Locate platelets.
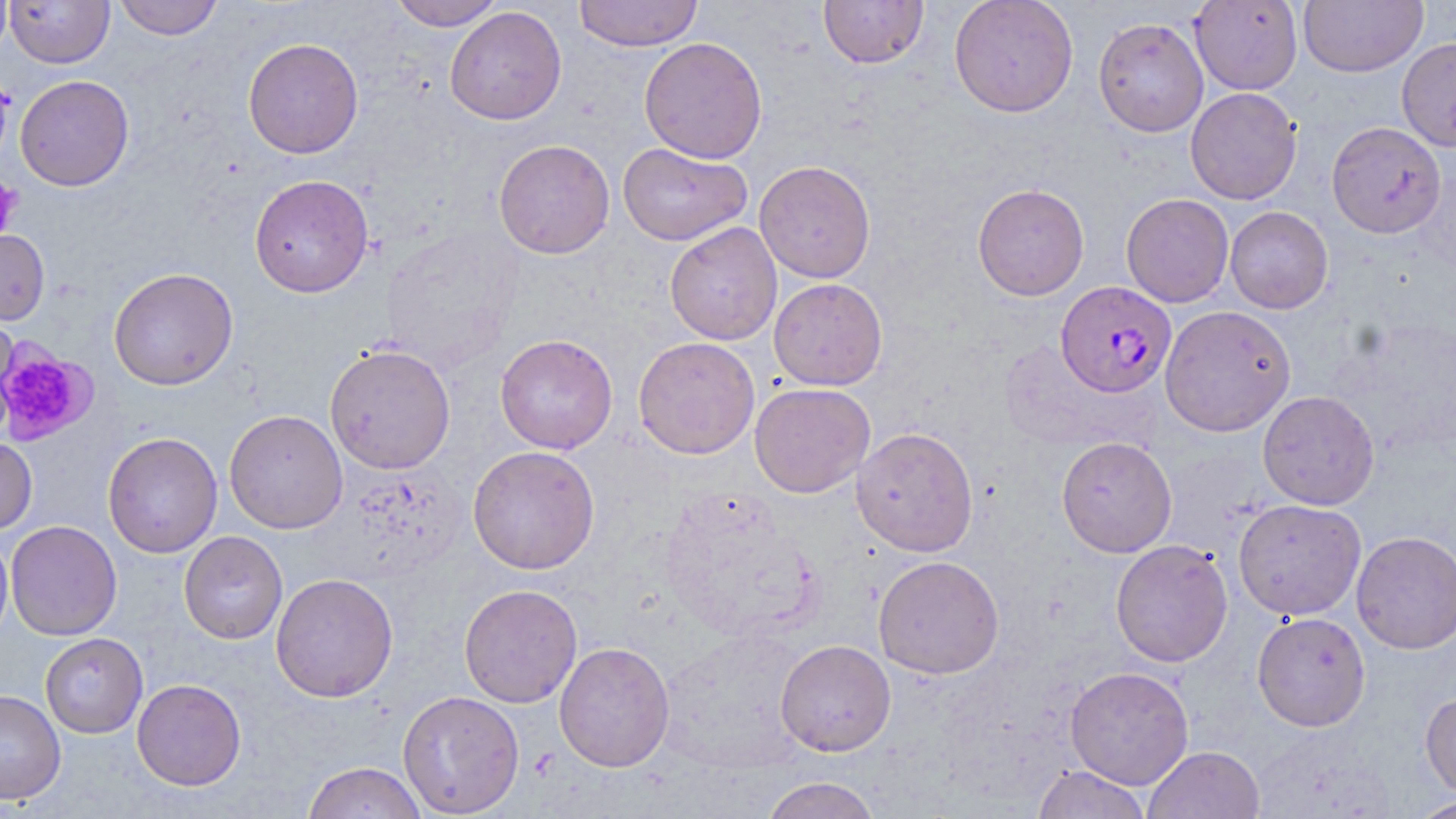

Approximate bounding boxes as named x1/y1/x2/y2 corners in pixels.
Platelets: (x1=0, y1=177, x2=22, y2=238), (x1=0, y1=340, x2=97, y2=447).

Summary:
  - Uninfected red blood cell locations: (x1=5, y1=0, x2=115, y2=68), (x1=114, y1=0, x2=223, y2=40), (x1=387, y1=0, x2=506, y2=30), (x1=573, y1=0, x2=704, y2=51), (x1=818, y1=0, x2=929, y2=69), (x1=949, y1=0, x2=1078, y2=117), (x1=1190, y1=1, x2=1302, y2=94), (x1=1298, y1=1, x2=1428, y2=76), (x1=444, y1=7, x2=566, y2=125), (x1=1093, y1=17, x2=1208, y2=137), (x1=639, y1=37, x2=767, y2=164), (x1=1397, y1=37, x2=1456, y2=151), (x1=243, y1=38, x2=363, y2=159), (x1=15, y1=74, x2=134, y2=191), (x1=1186, y1=87, x2=1302, y2=205), (x1=1326, y1=121, x2=1447, y2=238), (x1=493, y1=139, x2=615, y2=259), (x1=617, y1=143, x2=752, y2=246), (x1=754, y1=160, x2=876, y2=283), (x1=249, y1=174, x2=374, y2=298), (x1=972, y1=183, x2=1089, y2=300), (x1=1121, y1=193, x2=1234, y2=308), (x1=1225, y1=206, x2=1333, y2=313), (x1=664, y1=222, x2=782, y2=345), (x1=379, y1=226, x2=524, y2=372), (x1=0, y1=228, x2=49, y2=325), (x1=108, y1=267, x2=239, y2=390), (x1=769, y1=278, x2=888, y2=391), (x1=1159, y1=305, x2=1296, y2=436), (x1=0, y1=310, x2=19, y2=436), (x1=495, y1=334, x2=618, y2=454), (x1=633, y1=336, x2=760, y2=460), (x1=324, y1=343, x2=456, y2=475), (x1=749, y1=383, x2=875, y2=498), (x1=1257, y1=390, x2=1379, y2=510), (x1=224, y1=409, x2=347, y2=534), (x1=851, y1=427, x2=979, y2=557), (x1=102, y1=432, x2=223, y2=558), (x1=0, y1=436, x2=37, y2=535), (x1=1057, y1=436, x2=1177, y2=557), (x1=468, y1=445, x2=600, y2=575), (x1=1233, y1=498, x2=1366, y2=620), (x1=6, y1=520, x2=121, y2=641), (x1=1351, y1=530, x2=1456, y2=654), (x1=0, y1=531, x2=13, y2=652), (x1=179, y1=531, x2=287, y2=645), (x1=1110, y1=539, x2=1233, y2=668), (x1=873, y1=555, x2=1005, y2=679), (x1=270, y1=572, x2=399, y2=703), (x1=459, y1=584, x2=582, y2=708), (x1=1252, y1=612, x2=1371, y2=731), (x1=40, y1=633, x2=148, y2=739), (x1=775, y1=639, x2=896, y2=757), (x1=554, y1=642, x2=675, y2=772), (x1=1065, y1=666, x2=1194, y2=789), (x1=132, y1=678, x2=246, y2=791), (x1=0, y1=689, x2=66, y2=805), (x1=397, y1=690, x2=524, y2=818), (x1=1420, y1=691, x2=1456, y2=799), (x1=1249, y1=723, x2=1396, y2=818), (x1=1143, y1=746, x2=1265, y2=819), (x1=302, y1=761, x2=429, y2=819), (x1=1031, y1=765, x2=1152, y2=819), (x1=761, y1=776, x2=882, y2=819), (x1=1409, y1=795, x2=1456, y2=818)
  - Plasmodium falciparum-infected red blood cell locations: (x1=1055, y1=280, x2=1176, y2=397)
  - Slide-level diagnosis: Plasmodium falciparum
  - Field of view: single
  - Modality: light microscopy
  - Magnification: 1000x
  - Preparation: thin blood film
  - Image size: 1456×819 pixels
  - Stain: May-Grünwald-Giemsa